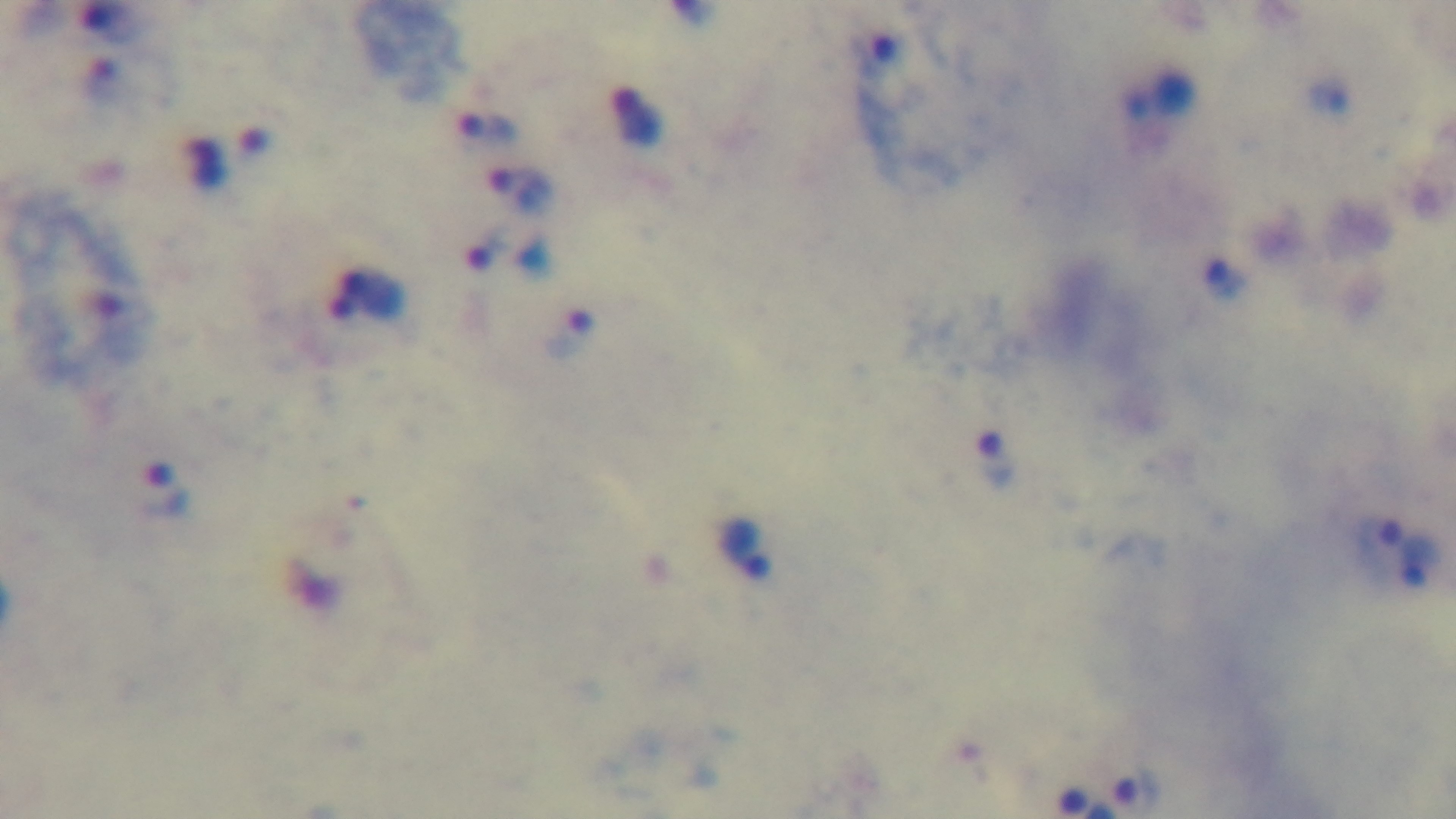

Mounted 4K digital camera. Malaria status: positive. One field from the slide. Giemsa-stained. Preparation: thick blood film. 100x oil-immersion objective. Light microscopy.